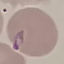

result = malaria parasites identified
capture = smartphone camera at the microscope eyepiece
stain = Giemsa
image type = cell patch, automatically extracted from a larger field of view and resized to 64 × 64 pixels
preparation = thin blood film